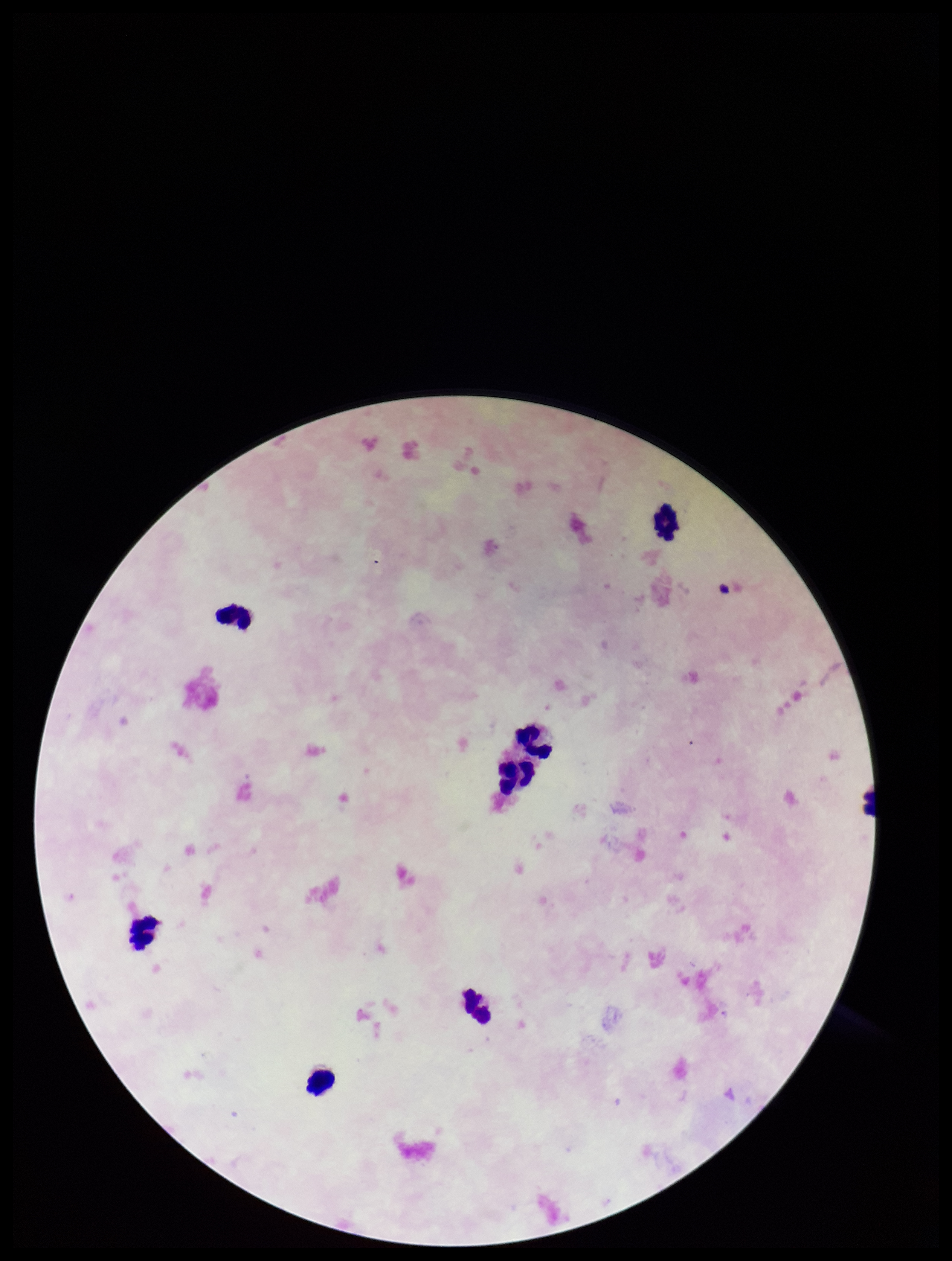

stain = Giemsa
image size = 952×1261 pixels
field of view = one from this slide
preparation = thick blood smear
Plasmodium parasites = none identified
leukocyte count = 7
parasite count = 0
patient malaria status = negative
capture = smartphone photograph through the microscope eyepiece